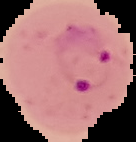

From a thin blood film. Cell region segmented out of the field of view; the surrounding area is masked to black. Image is 136×142 pixels. Result: Plasmodium parasites detected.